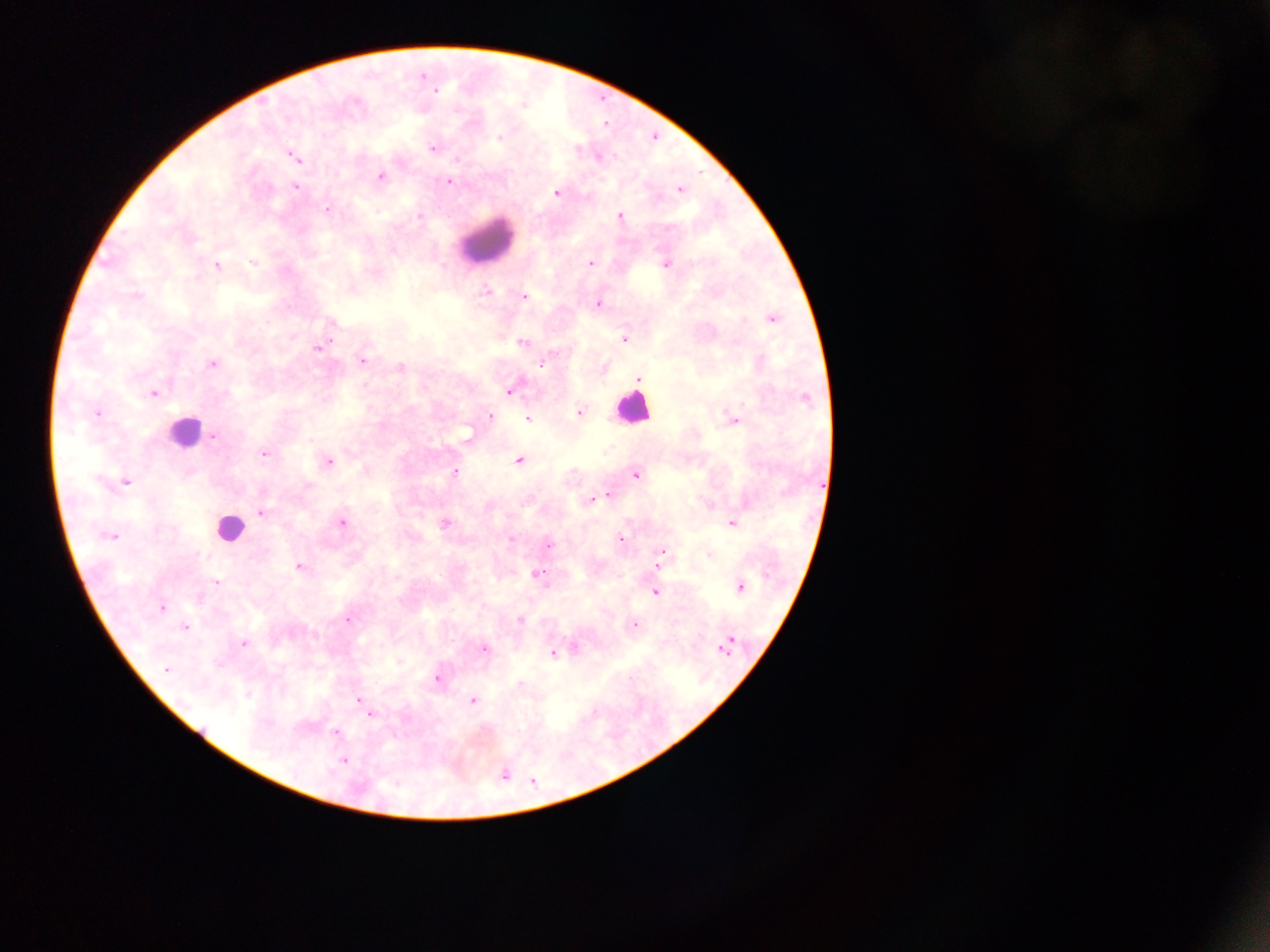
{
  "country": "Ghana",
  "leukocyte_locations": "approximate centers as (x, y) in pixels: (486, 242), (632, 408), (184, 431), (229, 529)",
  "capture": "mobile-phone photograph through a microscope",
  "malaria_parasite_locations": "approximate centers as (x, y) in pixels: (423, 77), (436, 90), (499, 137), (431, 148), (294, 157), (599, 157), (457, 159), (380, 176), (449, 182), (296, 187), (680, 189), (557, 192), (327, 209), (419, 216), (620, 216), (253, 262), (590, 263), (665, 264), (217, 266), (484, 291), (137, 296), (524, 296), (598, 304), (772, 319), (624, 339), (330, 340), (522, 343), (317, 348), (361, 360), (212, 365), (541, 365), (400, 367), (639, 378), (510, 391), (153, 394), (806, 398), (97, 413), (579, 413), (490, 416), (528, 419), (734, 420), (214, 437), (468, 438), (265, 454), (329, 461), (519, 461), (455, 472), (636, 475), (125, 482), (607, 497), (591, 500), (261, 513), (343, 524), (444, 524), (731, 524), (111, 537), (511, 539), (620, 539), (549, 544), (662, 551), (657, 565), (299, 566), (539, 574), (216, 582), (740, 588), (655, 592), (162, 609), (348, 619), (520, 620), (634, 626), (185, 627), (730, 642), (243, 643), (484, 648), (723, 648), (552, 653), (166, 669), (438, 679), (519, 683), (360, 699), (473, 700), (371, 714), (335, 732), (344, 761)",
  "preparation": "thick blood film",
  "image_size": "1270×952 pixels",
  "field_of_view": "single"
}